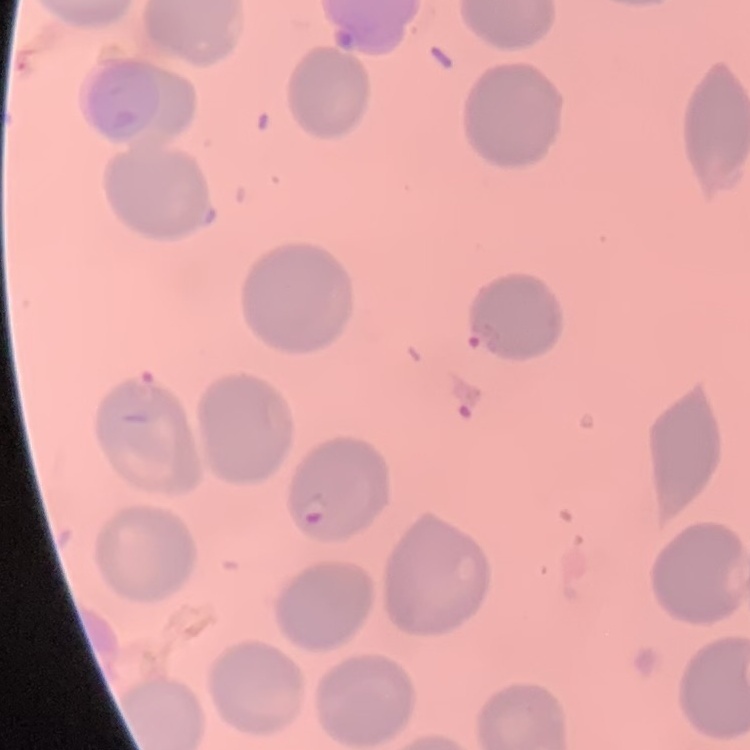 The erythrocytes show no rouleaux formation. Thin blood film. Stained with either Field's or Giemsa. One tile cut from a larger photomicrograph.